Assess this cell for malaria.
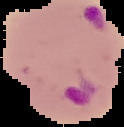

It is parasitized.

Summary:
  - Image size: 124×127 pixels
  - Image type: cell region segmented out of the field of view; surrounding area masked to black
  - Preparation: thin blood film